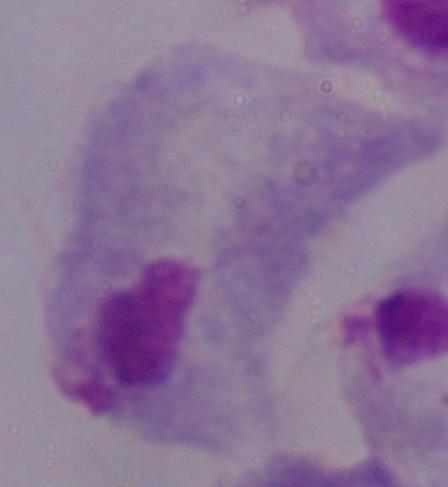

Micrograph. Captured at 1000x magnification. A trichomonad is shown.